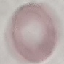
Summary:
  - Result: no malaria parasites detected
  - Stain: Giemsa
  - Preparation: thin blood smear
  - Image type: automatically extracted cell patch, resized to 64 × 64 pixels
  - Capture: smartphone camera at the microscope eyepiece